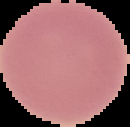
Segmented cell region on a black background. Result: negative for malaria parasites. From a thin blood smear. Image is 130×127 pixels.